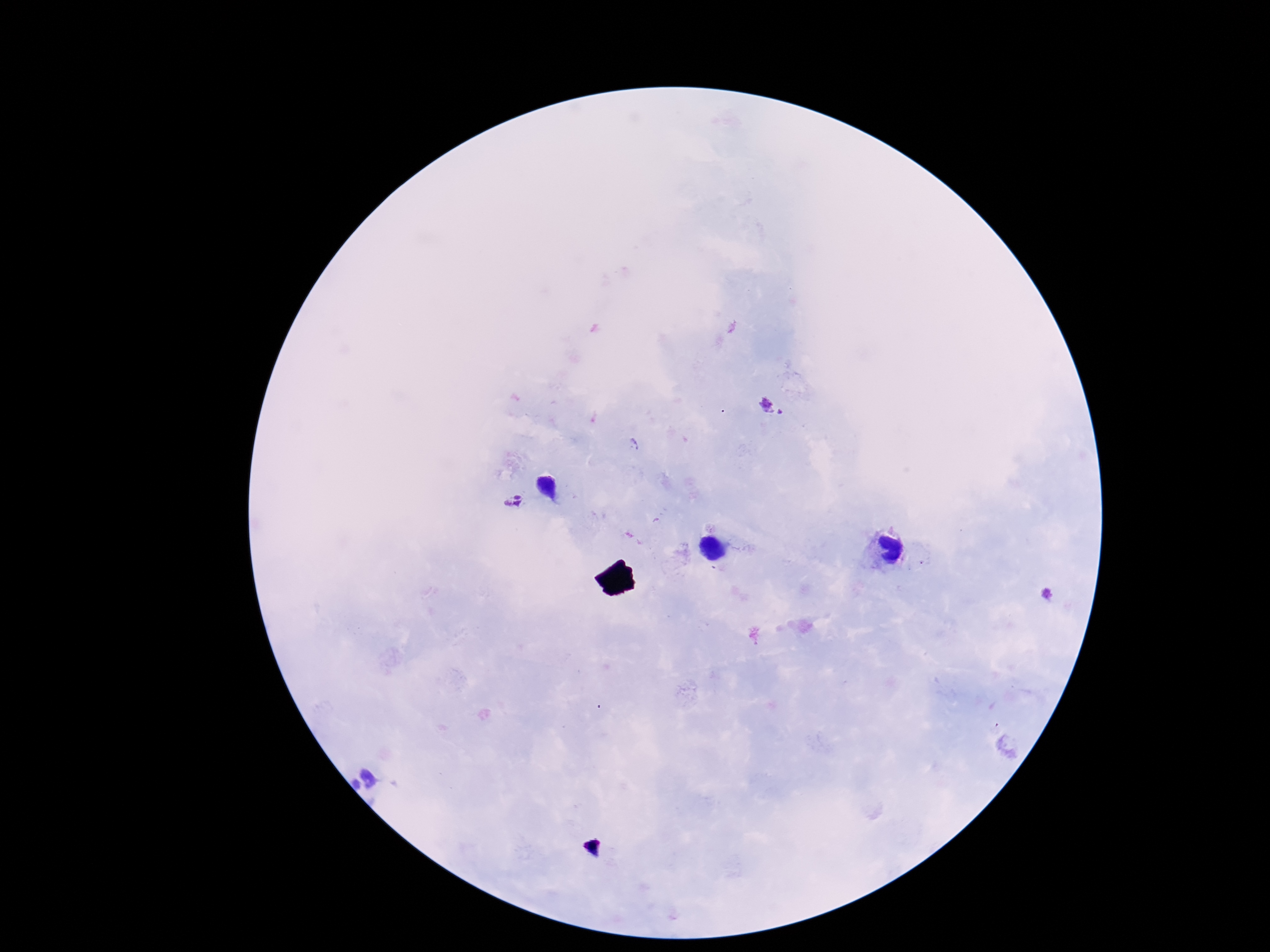

Approximate object centers, in pixels from the top-left corner. Plasmodium parasite locations: (x=769, y=407), (x=513, y=503), (x=1049, y=594). Giemsa stain. Patient malaria status: positive. Smartphone photograph taken through the microscope eyepiece. 100x magnification. Image is 1270×952 pixels. Thick blood smear. One field from this slide.